Assess the morphology of the erythrocytes.
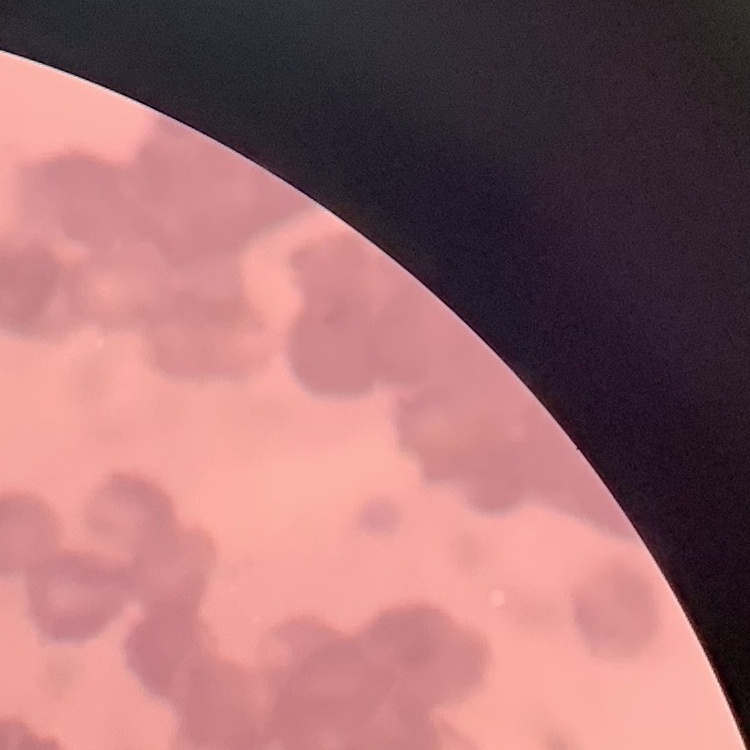
Rouleaux formation.

Thin blood film. Field's or Giemsa stain. Square crop of a larger photomicrograph.